Name the cell type shown.
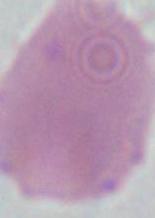

This is an erythrocyte.

1000x magnification. Micrograph.